Name the cell type shown.
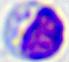

A leukocyte.

Summary:
  - Magnification: 400x
  - Modality: photomicrograph